Identify the parasite.
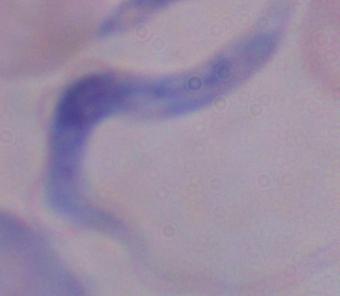
A trypanosome.

magnification: 1000x
modality: micrograph